Locate every parasitized red blood cell.
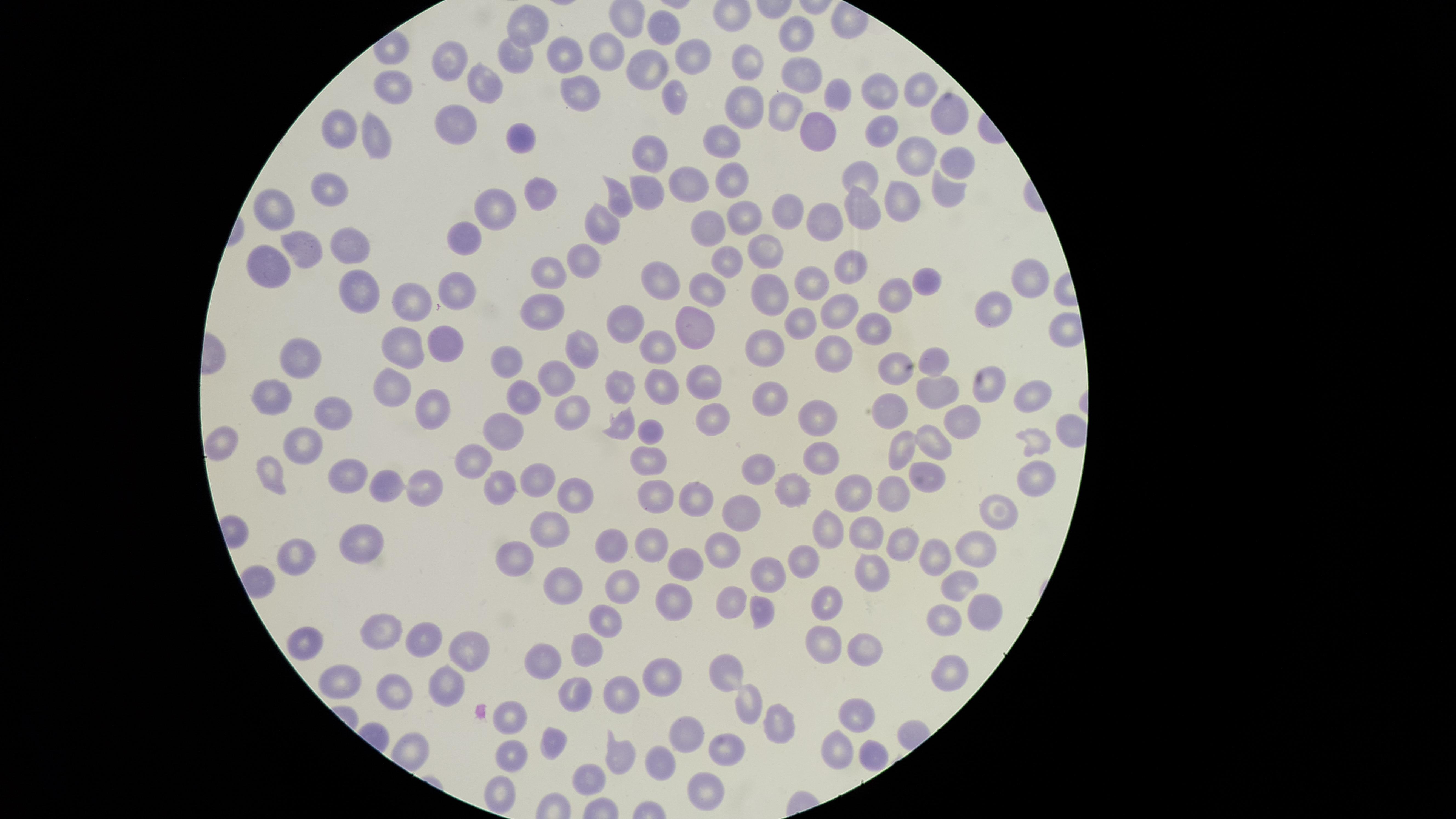

No parasitized red blood cells identified.

capture = smartphone photograph through the microscope eyepiece
image size = 1456×819 pixels
preparation = thin blood smear
stain = Giemsa
uninfected red blood cells = approximate marker points as (x, y) in pixels: (528, 25), (662, 32), (799, 35), (609, 46), (566, 51), (512, 55), (451, 58), (693, 58), (750, 62), (647, 68), (801, 73), (479, 82), (920, 84), (394, 90), (882, 91), (576, 94), (845, 96), (672, 97), (747, 105), (781, 111), (955, 115), (457, 123), (343, 124), (815, 127), (878, 130), (375, 138), (521, 139), (729, 139), (909, 150), (651, 155), (952, 162), (866, 175), (685, 180), (733, 181), (333, 186), (647, 188), (945, 189), (623, 195), (544, 196), (902, 199), (272, 203), (496, 206), (792, 211), (860, 212), (748, 213), (822, 221), (717, 223), (606, 224), (467, 235), (347, 242), (766, 246), (303, 248), (588, 251), (729, 259), (263, 261), (857, 262), (546, 273), (1030, 275), (648, 283), (362, 284), (920, 284), (824, 285), (458, 286), (712, 286), (771, 292), (898, 295), (409, 301), (540, 308), (992, 308), (832, 312), (624, 321), (796, 322), (871, 326), (692, 328), (447, 340), (402, 342), (836, 345), (660, 348), (768, 349), (586, 350), (308, 358), (935, 360), (509, 362), (893, 365), (554, 372), (390, 380), (664, 380), (707, 380), (625, 386), (989, 386), (1027, 391), (269, 395), (937, 395), (518, 398), (771, 399), (569, 409), (334, 410), (712, 412), (421, 416), (821, 417), (894, 417), (625, 421), (968, 423), (503, 426), (656, 429), (307, 437), (935, 437), (1035, 439), (219, 441), (905, 443), (820, 457), (650, 458), (470, 464), (924, 469), (760, 470), (354, 472), (1032, 476), (272, 478), (533, 481), (894, 485), (391, 486), (431, 486), (496, 488), (790, 488), (855, 488), (570, 495), (650, 495), (694, 503), (741, 510), (994, 514), (550, 528), (827, 532), (866, 532), (895, 540), (606, 541), (648, 543), (358, 544), (978, 546), (721, 549), (937, 549), (294, 556), (802, 558), (516, 559), (683, 562), (872, 569), (763, 572), (956, 580), (566, 581), (625, 585), (727, 598), (674, 601), (831, 603), (986, 609), (758, 610), (947, 617), (605, 619), (380, 630), (427, 637), (822, 642), (867, 645), (587, 648), (467, 655), (547, 655), (728, 671), (660, 673), (948, 674), (341, 680), (441, 686), (626, 687), (388, 689), (576, 691), (750, 705), (857, 710), (516, 716), (779, 725), (686, 733), (556, 740), (725, 748), (841, 748), (510, 753), (871, 756), (623, 757), (660, 764), (592, 778), (701, 789), (497, 794)
field of view = single
visible region = circular